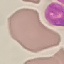 Result: no malaria parasites detected. Thin blood smear. Automatically extracted cell patch, resized to 64 × 64 pixels. Acquired by smartphone through the microscope eyepiece. Giemsa-stained preparation.